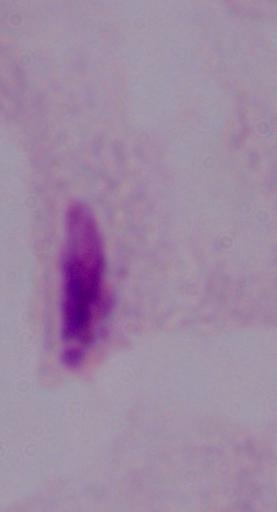
Photomicrograph. 1000x magnification. A trichomonad is seen.